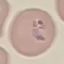
malaria status = parasitized
preparation = thin smear
stain = Giemsa
capture = smartphone through the microscope eyepiece
image type = automatically extracted cell patch, resized to 64 × 64 pixels